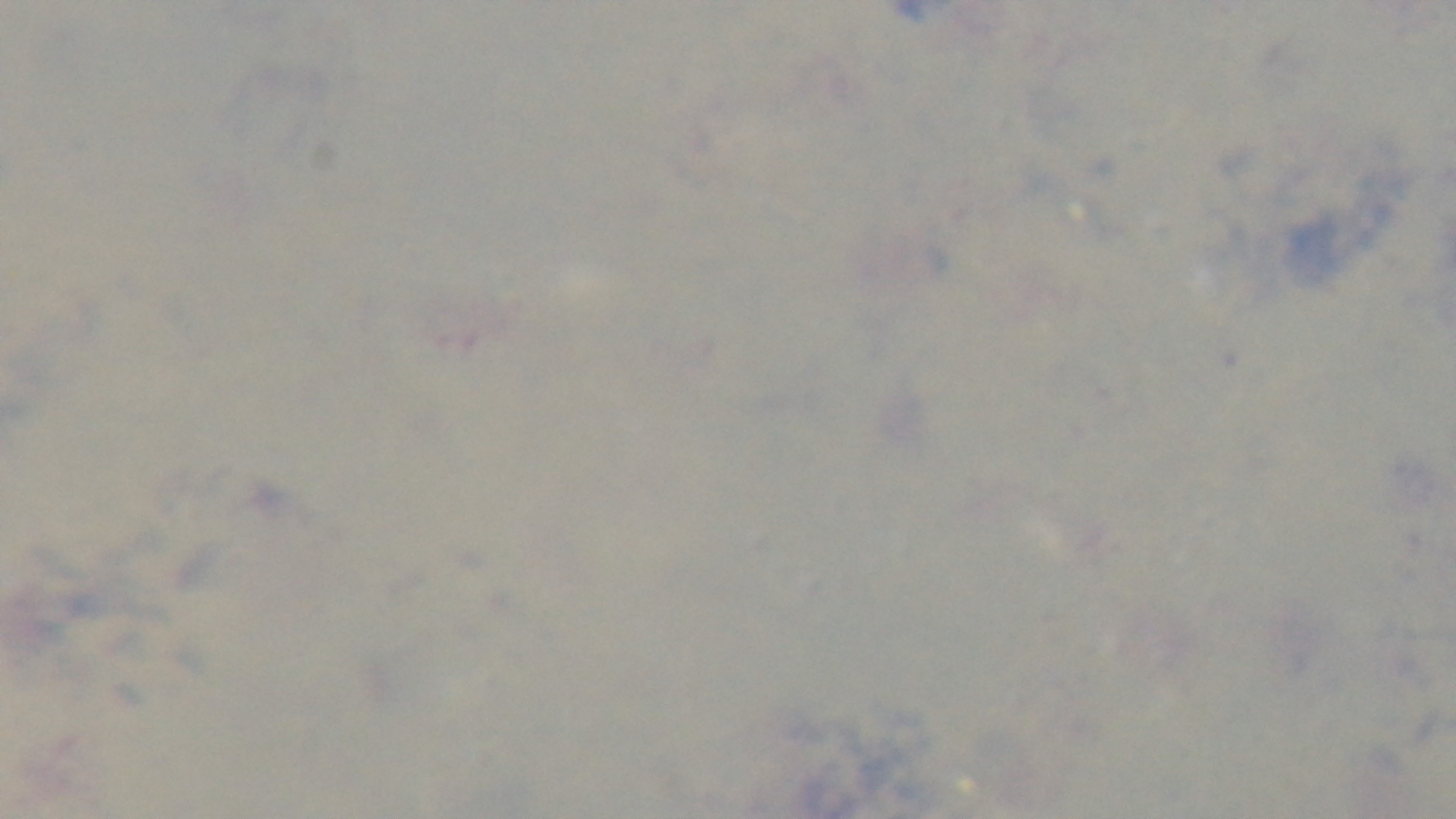
Summary:
  - Field of view: one from the slide
  - Stain: Giemsa
  - Capture: mounted 4K digital camera
  - Preparation: thick smear
  - Modality: light microscopy
  - Malaria status: negative
  - Objective: 100x oil immersion